Comment on the morphology of the erythrocytes.
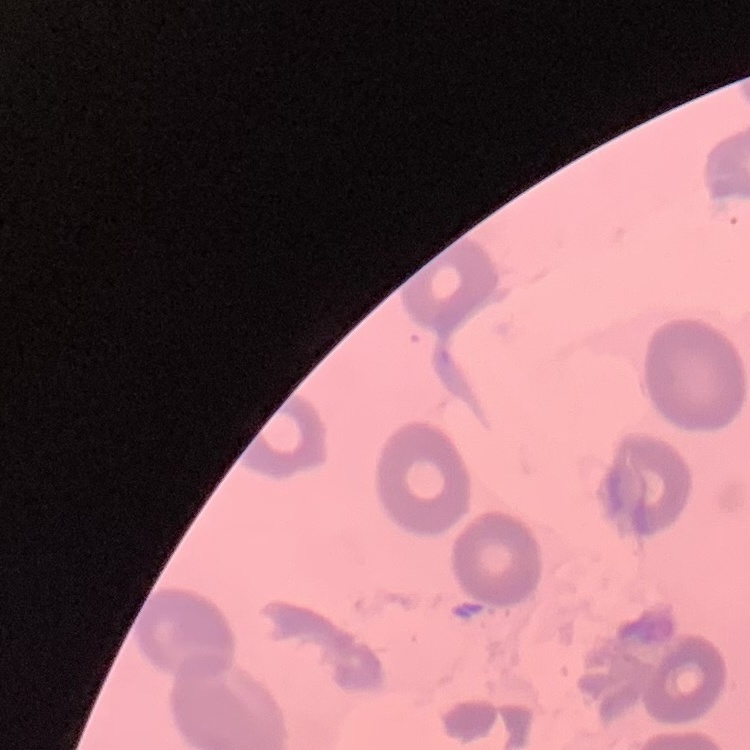
No rouleaux formation.

Stained with either Field's or Giemsa. Square crop of a larger photomicrograph. Thin peripheral smear.